Give the extent of all uninfected red blood cells.
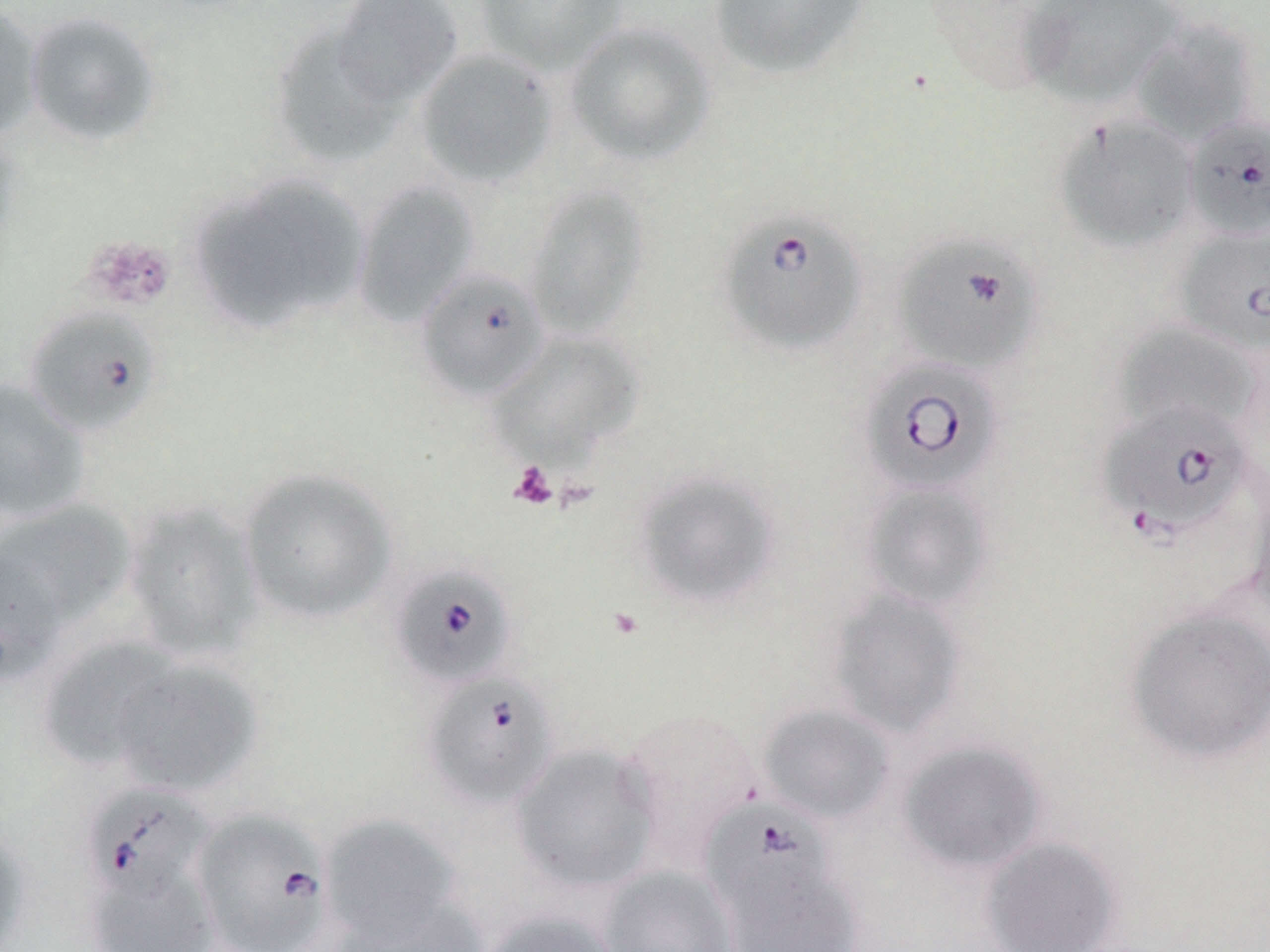
Approximate bounding boxes as (x1, y1, x2, y2) in pixels.
Uninfected red blood cells: (329, 0, 464, 107), (474, 0, 627, 74), (708, 0, 872, 80), (1019, 0, 1185, 109), (0, 3, 43, 141), (23, 11, 164, 147), (1129, 19, 1260, 146), (565, 21, 716, 165), (270, 22, 402, 169), (415, 49, 557, 187), (1054, 115, 1199, 252), (191, 176, 368, 334), (352, 181, 480, 326), (522, 185, 649, 338), (1114, 322, 1261, 439), (489, 330, 644, 469), (0, 380, 91, 523), (238, 467, 397, 624), (632, 469, 781, 610), (1245, 479, 1270, 622), (859, 480, 995, 612), (1, 501, 137, 630), (123, 501, 264, 661), (0, 547, 63, 688), (827, 588, 968, 737), (1125, 605, 1270, 766), (38, 637, 182, 771), (110, 658, 262, 796), (758, 703, 895, 825), (615, 708, 764, 865), (897, 740, 1047, 874), (510, 743, 660, 893), (319, 815, 467, 945), (0, 821, 33, 952), (979, 836, 1123, 952), (83, 864, 219, 951), (598, 865, 740, 952), (722, 865, 864, 952), (331, 895, 489, 952), (478, 909, 624, 952).

{
  "slide_level_diagnosis": "Babesia divergens",
  "stain": "May-Grünwald-Giemsa",
  "field_of_view": "single",
  "preparation": "thin blood smear",
  "modality": "optical microscopy",
  "magnification": "1000x",
  "babesia_divergens_infected_red_blood_cell_locations": "approximate bounding boxes as (x1, y1, x2, y2) in pixels: (1183, 114, 1270, 241), (717, 208, 867, 356), (1176, 225, 1270, 356), (892, 233, 1043, 376), (416, 267, 550, 402), (24, 306, 163, 436), (859, 357, 1004, 496), (1098, 402, 1255, 541), (390, 562, 518, 689), (423, 672, 560, 810), (81, 782, 214, 905), (701, 799, 838, 925), (191, 808, 334, 952)",
  "platelet_locations": "approximate bounding boxes as (x1, y1, x2, y2) in pixels: (81, 234, 177, 312), (508, 461, 559, 510)",
  "image_size": "1270×952 pixels"
}